Assess this cell for malaria.
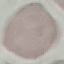

Uninfected.

image type = cell patch, automatically extracted from a larger field of view and resized to 64 × 64 pixels
capture = smartphone through the microscope eyepiece
preparation = thin blood smear
stain = Giemsa